State which parasite is depicted.
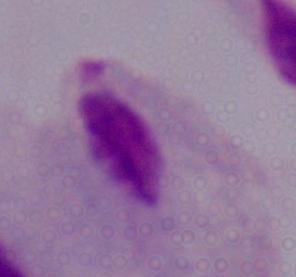
A trichomonad.

Captured at 1000x magnification. Micrograph.